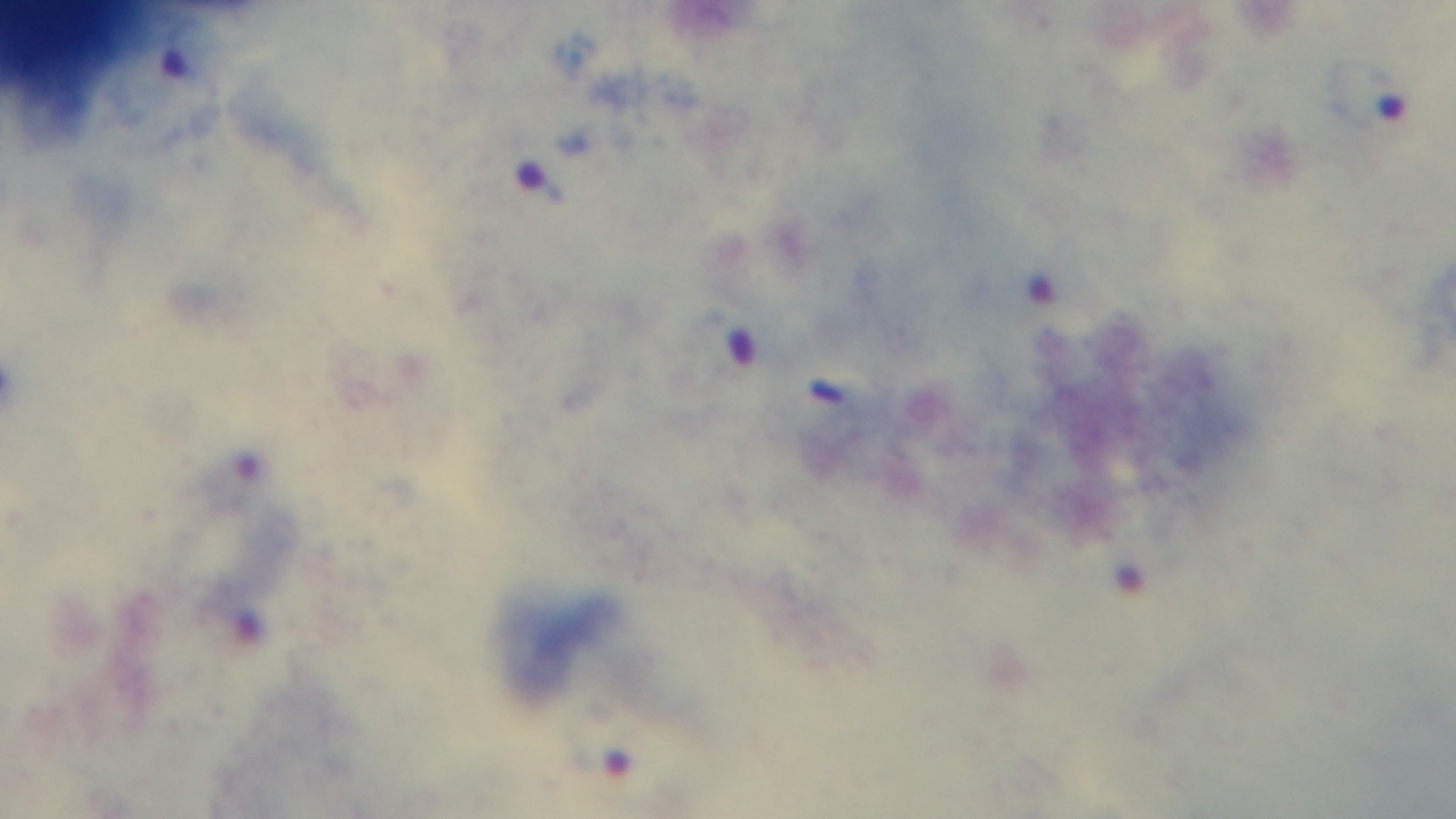 Preparation: thick blood film. One field from the slide. Photomicrograph. Oil-immersion objective, 100x. Giemsa stain. Malaria status: infected. Captured with a mounted 4K digital camera.